Assess this cell for malaria.
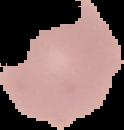

Uninfected.

preparation: thin blood film
image_type: segmented cell region with the area outside set to black
image_size: 124×130 pixels